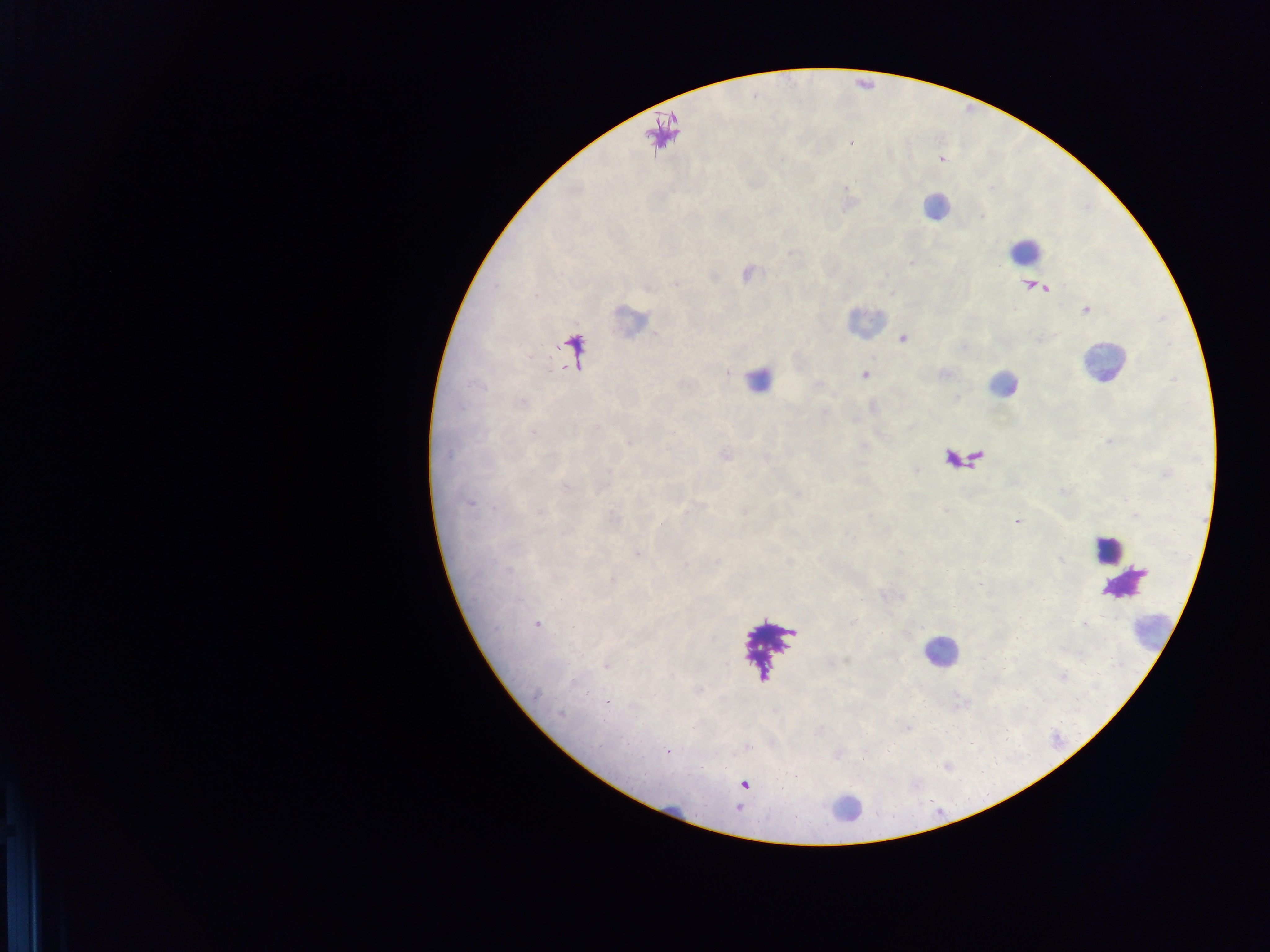

Approximate centers as (x, y) in pixels.
Summary:
  - Malaria parasite locations: (902, 338), (864, 375), (1017, 521), (638, 553), (536, 625), (606, 666), (560, 713), (748, 747), (668, 751), (744, 785)
  - Leukocyte locations: (936, 206), (1024, 250), (1101, 363), (760, 369), (1108, 549), (1123, 577), (939, 651)
  - Field of view: single
  - Preparation: thick blood smear
  - Capture: mobile-phone photograph through a microscope
  - Image size: 1270×952 pixels
  - Country: Ghana